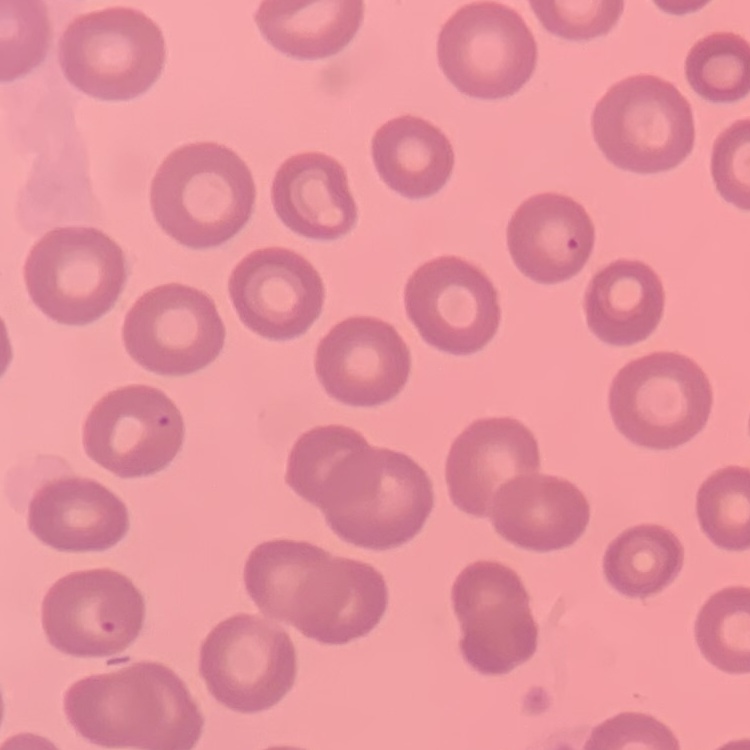
Summary:
  - Red blood cell morphology: no rouleaux formation
  - Preparation: thin peripheral smear
  - Stain: Field's or Giemsa
  - Image type: one tile cut from a larger photomicrograph